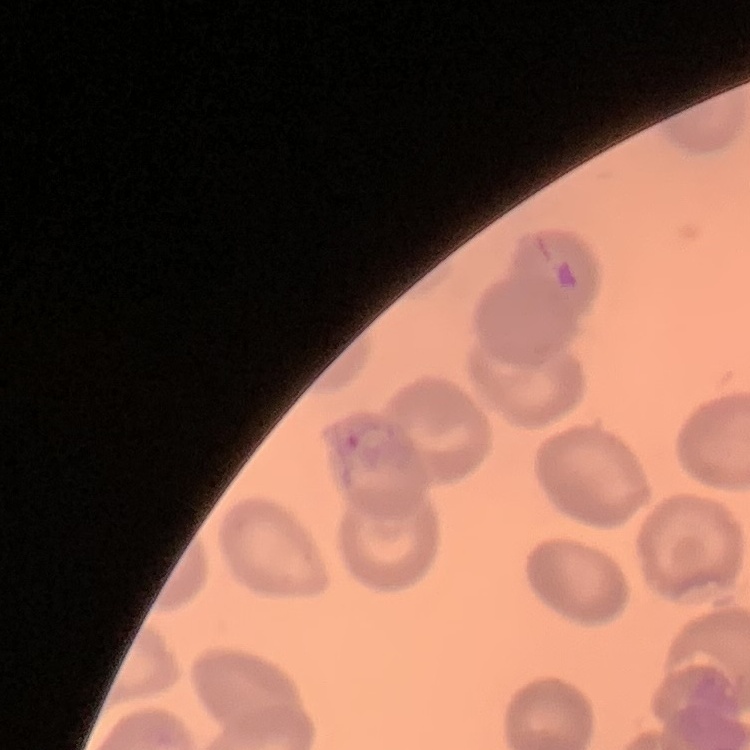
red blood cell morphology = no rouleaux formation
image type = square crop of a larger photomicrograph
preparation = thin blood smear
stain = Field's or Giemsa